Outline each blood parasite and name the species.
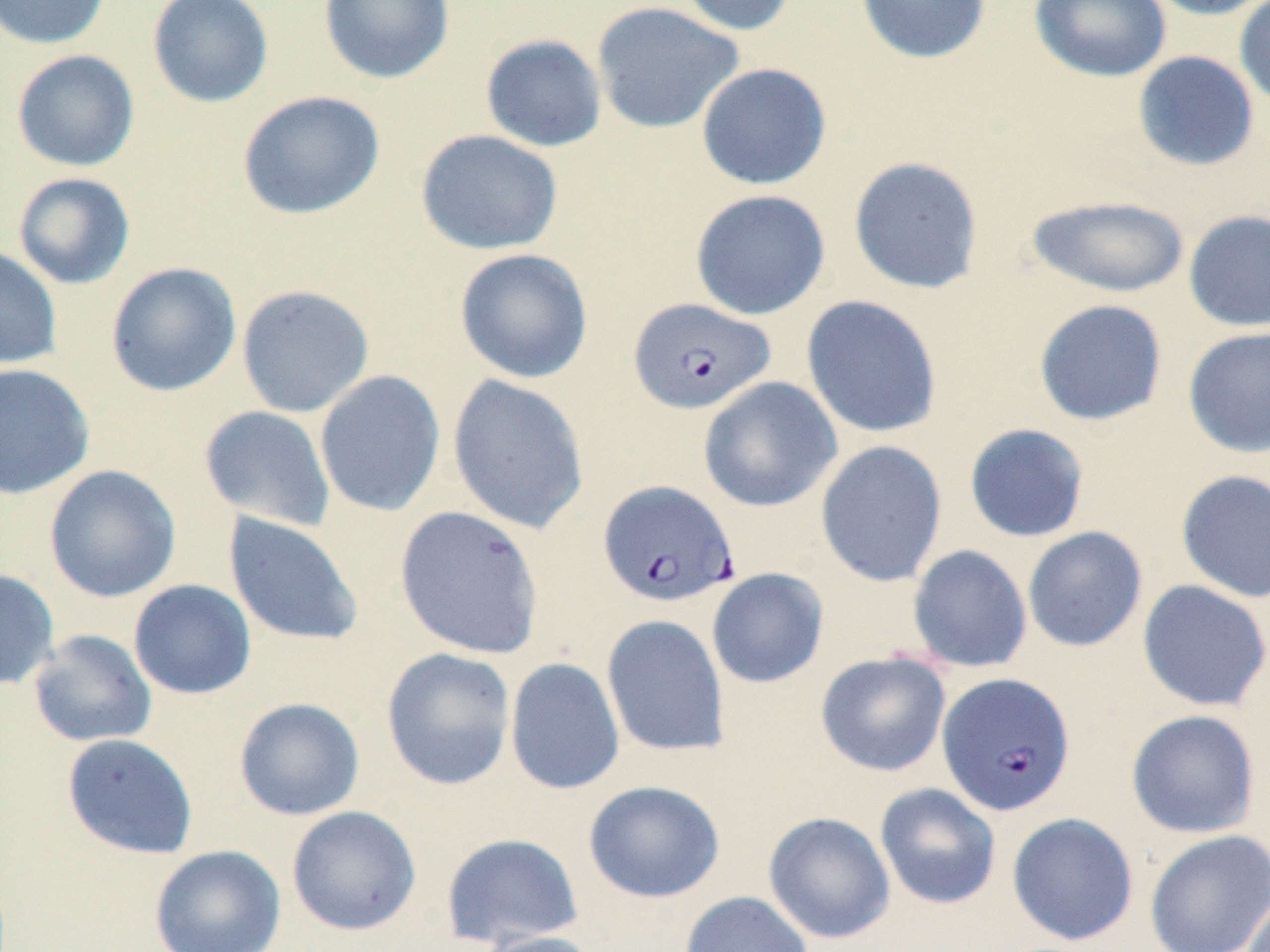
Approximate bounding boxes as (x1, y1, x2, y2) in pixels.
Plasmodium falciparum-infected red blood cells: (629, 297, 775, 415), (598, 479, 739, 608), (938, 672, 1075, 816).
No Plasmodium ovale, Plasmodium malariae, Plasmodium vivax, Babesia divergens, or Trypanosoma brucei observed.

slide-level diagnosis = Plasmodium falciparum
image size = 1270×952 pixels
field of view = single
preparation = thin blood smear
stain = May-Grünwald-Giemsa
uninfected red blood cell locations = approximate bounding boxes as (x1, y1, x2, y2) in pixels: (0, 0, 112, 50), (147, 0, 274, 108), (318, 0, 455, 84), (673, 0, 799, 36), (854, 0, 992, 65), (1029, 0, 1172, 83), (1140, 0, 1270, 20), (1233, 0, 1270, 112), (591, 1, 745, 135), (479, 34, 608, 153), (11, 49, 140, 172), (1132, 51, 1260, 171), (696, 62, 832, 190), (237, 90, 385, 220), (415, 129, 563, 256), (848, 156, 984, 295), (12, 172, 136, 290), (690, 189, 830, 320), (1026, 195, 1190, 298), (1183, 209, 1270, 332), (0, 244, 62, 370), (454, 248, 594, 384), (105, 261, 242, 398), (236, 284, 375, 418), (800, 294, 943, 439), (1033, 299, 1168, 426), (1182, 326, 1270, 459), (0, 363, 95, 500), (314, 370, 446, 517), (447, 373, 590, 536), (698, 377, 842, 512), (199, 405, 337, 533), (963, 423, 1090, 543), (815, 440, 948, 587), (44, 465, 181, 603), (1175, 469, 1270, 603), (394, 506, 544, 660), (223, 513, 364, 647), (1022, 526, 1148, 652), (907, 544, 1033, 673), (0, 568, 59, 690), (706, 568, 829, 688), (128, 579, 256, 700), (1137, 579, 1270, 712), (601, 615, 730, 758), (28, 629, 157, 747), (381, 647, 517, 790), (815, 650, 952, 777), (505, 657, 625, 795), (233, 697, 365, 820), (1126, 709, 1262, 838), (62, 733, 198, 859), (582, 780, 725, 904), (874, 782, 1002, 910), (286, 805, 421, 936), (763, 811, 896, 944), (1006, 812, 1139, 946), (1144, 830, 1270, 952), (440, 832, 584, 949), (149, 845, 286, 952), (1240, 886, 1270, 952), (679, 890, 813, 952), (473, 930, 605, 952)
magnification = 1000x
modality = light microscopy